Locate every blood parasite and identify its species.
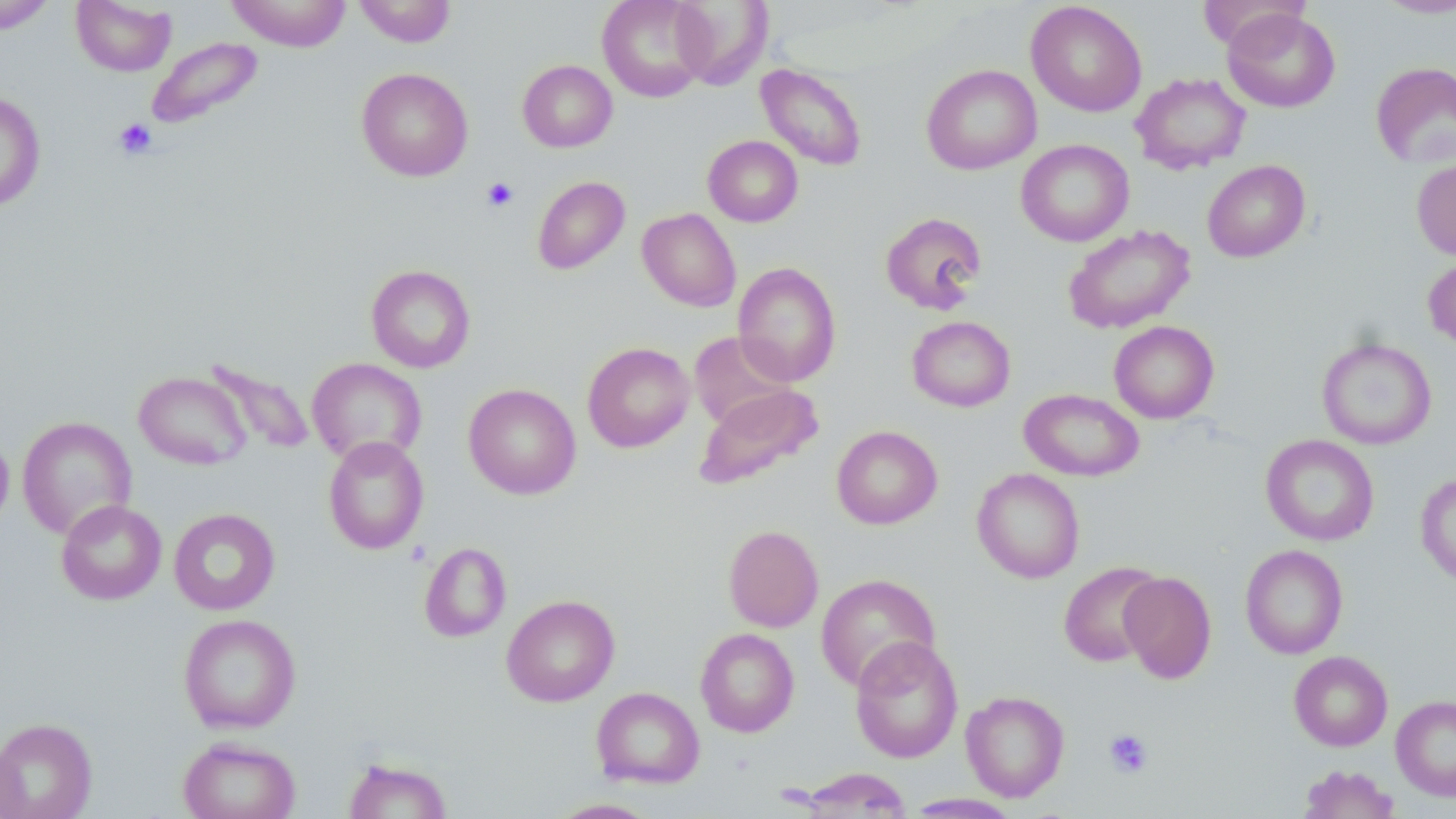
No blood parasites observed.

slide-level diagnosis = no evidence of blood parasites
magnification = 1000x
modality = optical microscopy
image size = 1456×819 pixels
stain = May-Grünwald-Giemsa
uninfected red blood cell locations = approximate bounding boxes as (x1,y1)-(x2,y2) corner pairs in pixels: (71,0)-(177,76), (225,0)-(352,51), (353,0)-(456,47), (596,0)-(713,102), (670,0)-(772,90), (1373,0)-(1456,18), (1026,1)-(1147,117), (0,3)-(57,35), (1222,8)-(1340,112), (146,37)-(264,128), (518,60)-(617,152), (1371,61)-(1456,169), (755,63)-(869,171), (921,64)-(1042,174), (357,67)-(473,181), (1130,72)-(1251,175), (0,90)-(46,211), (703,135)-(803,227), (1016,139)-(1134,246), (1411,159)-(1456,261), (1202,160)-(1310,262), (532,176)-(630,274), (637,208)-(741,311), (880,211)-(987,315), (1063,224)-(1195,334), (1422,255)-(1456,351), (732,261)-(841,387), (366,264)-(476,373), (907,316)-(1016,412), (1108,321)-(1219,423), (689,331)-(798,432), (1317,337)-(1437,450), (582,341)-(695,452), (204,357)-(316,457), (307,358)-(427,466), (134,371)-(251,469), (464,383)-(581,499), (694,383)-(824,490), (1019,389)-(1144,481), (17,415)-(137,539), (831,425)-(942,529), (0,431)-(14,536), (1261,434)-(1379,546), (322,436)-(429,555), (972,468)-(1085,583), (1415,472)-(1456,588), (56,499)-(167,604), (169,507)-(280,615), (723,524)-(823,632), (419,542)-(511,642), (1240,544)-(1348,659), (1058,561)-(1164,667), (1119,571)-(1217,683), (815,574)-(941,691), (501,594)-(619,707), (178,613)-(302,733), (695,628)-(799,737), (849,636)-(964,763), (1289,650)-(1393,751), (591,687)-(704,789), (961,690)-(1070,801), (1391,694)-(1456,801), (0,717)-(98,819), (178,736)-(301,819), (0,737)-(25,819), (342,757)-(453,819), (1298,764)-(1399,818), (794,768)-(914,818), (904,793)-(1022,818), (546,798)-(663,818)
field of view = one of a larger specimen
platelet locations = approximate bounding boxes as (x1,y1)-(x2,y2) corner pairs in pixels: (113,118)-(157,159), (482,178)-(518,212), (1103,728)-(1154,778)
preparation = thin blood film